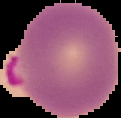
Summary:
  - Preparation: thin blood smear
  - Image size: 121×118 pixels
  - Image type: segmented cell region on a black background
  - Result: malaria parasites identified